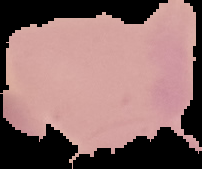

image size = 202×169 pixels
image type = segmented cell region on a black background
result = no Plasmodium parasites seen
preparation = thin blood smear